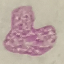 Result: negative for malaria parasites. Giemsa-stained preparation. Photographed with a smartphone camera at the microscope eyepiece. Thin blood smear. Cell patch, automatically extracted from a larger field of view and resized to 64 × 64 pixels.